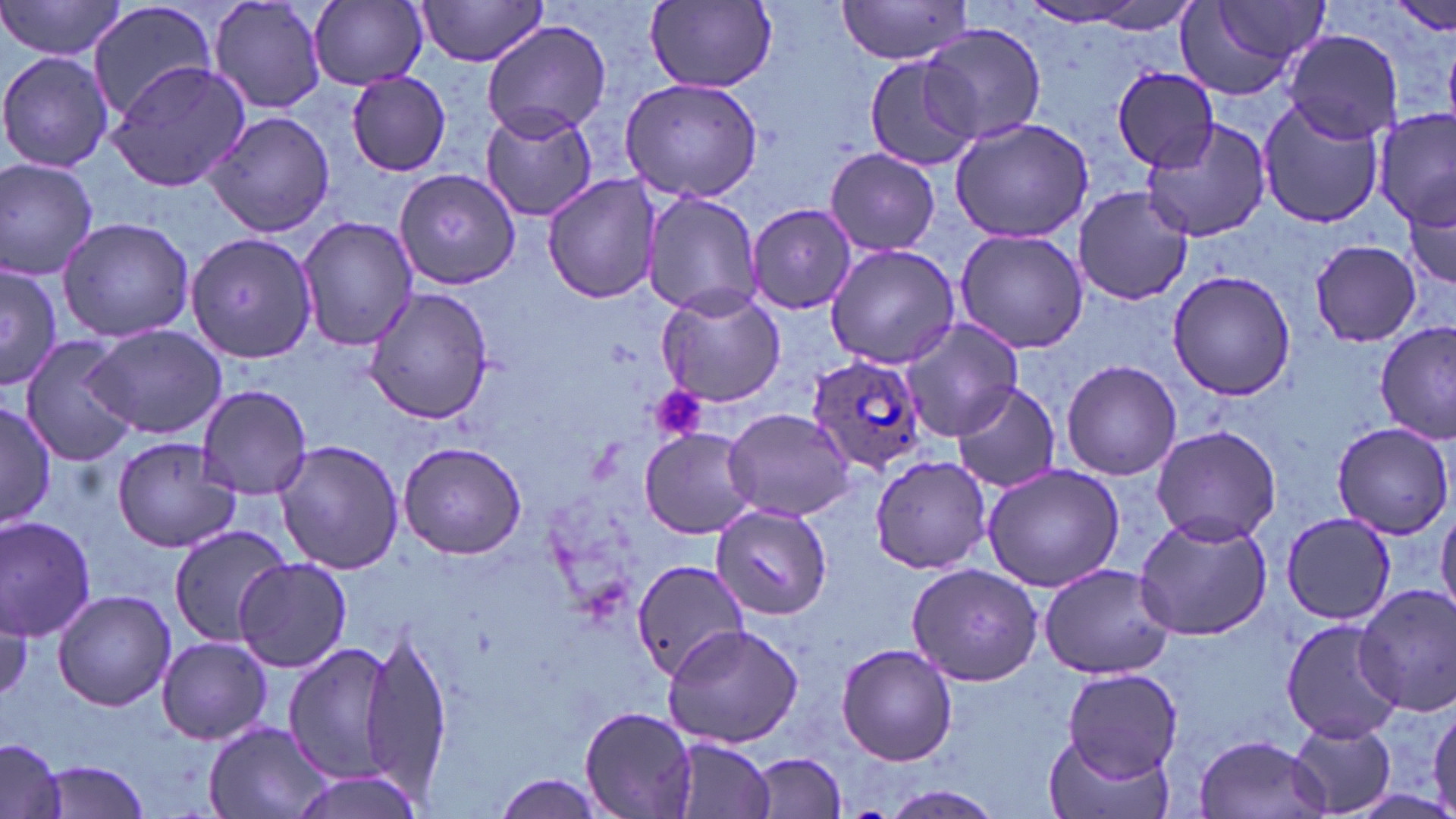
Summary:
  - Coordinate format: approximate bounding boxes as (x1, y1, x2, y2) in pixels
  - Plasmodium ovale-infected red blood cell locations: (807, 354, 927, 475)
  - Uninfected red blood cell locations: (0, 0, 129, 63), (207, 0, 329, 115), (85, 1, 221, 122), (308, 1, 427, 88), (413, 1, 553, 68), (647, 1, 778, 90), (833, 1, 974, 64), (1178, 1, 1327, 98), (1014, 3, 1159, 28), (480, 19, 611, 140), (921, 25, 1047, 146), (1284, 30, 1401, 142), (0, 50, 115, 173), (862, 53, 985, 171), (104, 60, 252, 193), (1112, 68, 1221, 172), (345, 69, 452, 175), (619, 77, 767, 205), (1256, 100, 1386, 229), (479, 105, 597, 223), (1375, 108, 1455, 235), (199, 109, 336, 238), (948, 117, 1094, 242), (1140, 120, 1274, 244), (824, 148, 941, 257), (0, 156, 100, 280), (393, 170, 519, 287), (542, 173, 663, 305), (1405, 185, 1455, 300), (1073, 186, 1192, 306), (641, 191, 763, 316), (749, 203, 859, 314), (296, 214, 417, 349), (57, 215, 198, 342), (954, 228, 1089, 354), (185, 232, 319, 364), (1306, 238, 1424, 348), (825, 243, 964, 368), (0, 264, 62, 389), (1167, 270, 1296, 401), (361, 285, 496, 425), (655, 287, 786, 407), (897, 316, 1024, 442), (84, 323, 228, 441), (1374, 323, 1454, 443), (20, 336, 142, 465), (1062, 358, 1181, 481), (947, 381, 1062, 496), (196, 385, 313, 498), (0, 395, 57, 531), (723, 407, 855, 523), (1331, 421, 1453, 538), (1149, 425, 1281, 546), (638, 428, 757, 538), (110, 434, 243, 553), (274, 439, 406, 576), (397, 439, 526, 561), (869, 453, 994, 574), (981, 462, 1128, 592), (711, 505, 832, 619), (1436, 506, 1456, 620), (1280, 512, 1395, 626), (0, 514, 99, 641), (1132, 514, 1274, 642), (166, 525, 293, 645), (235, 558, 351, 673), (628, 558, 748, 683), (1037, 562, 1175, 679), (905, 563, 1043, 684), (1352, 583, 1456, 718), (53, 590, 176, 711), (1282, 617, 1399, 742), (662, 624, 805, 748), (359, 627, 453, 802), (155, 635, 272, 745), (281, 640, 400, 785), (836, 642, 958, 767), (1062, 668, 1182, 779), (1428, 700, 1456, 816), (578, 704, 699, 819), (1286, 718, 1397, 816), (202, 720, 334, 819), (1041, 730, 1170, 819), (1192, 733, 1330, 819), (669, 736, 777, 819), (0, 740, 68, 819), (751, 752, 846, 816), (34, 759, 153, 817), (285, 769, 427, 818), (490, 775, 612, 818), (877, 787, 1006, 819)
  - Platelet locations: (649, 387, 707, 445)
  - Slide-level diagnosis: Plasmodium ovale
  - Stain: May-Grünwald-Giemsa
  - Preparation: thin blood smear
  - Image size: 1456×819 pixels
  - Modality: optical microscopy
  - Field of view: one of a larger specimen
  - Magnification: 1000x